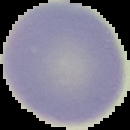

result = negative for malaria parasites
image type = segmented cell region with the area outside set to black
image size = 130×130 pixels
preparation = thin blood film